Report the malaria status of this cell.
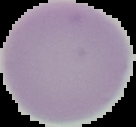
It is uninfected.

Summary:
  - Image size: 136×127 pixels
  - Preparation: thin blood film
  - Image type: segmented cell region on a black background